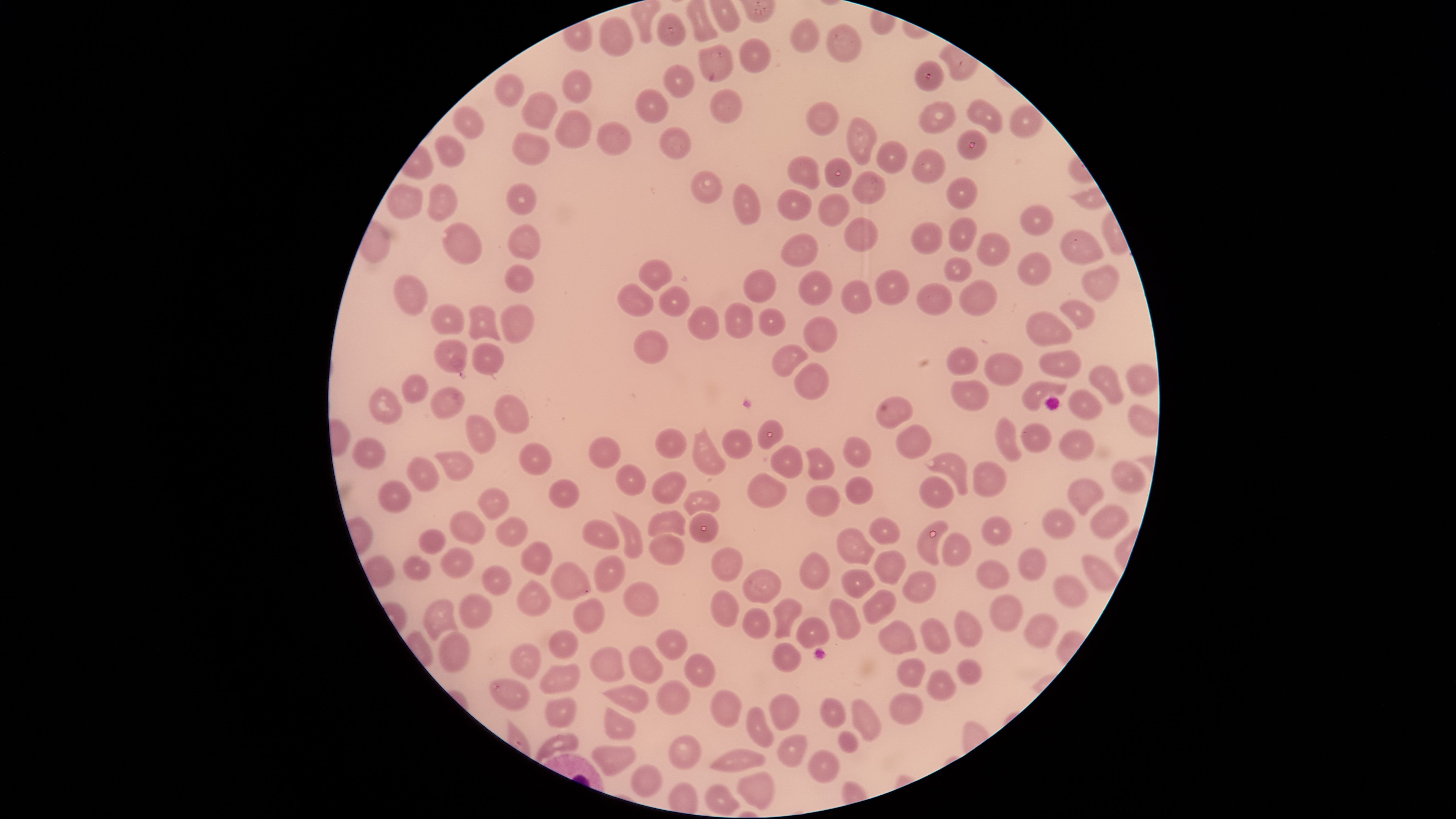 Approximate bounding boxes as [left, top, right, bottom] in pixels. Uninfected red blood cells: [655, 11, 687, 48], [599, 15, 634, 57], [788, 16, 820, 53], [825, 23, 863, 64], [739, 37, 771, 74], [696, 43, 734, 84], [914, 59, 945, 93], [662, 64, 695, 98], [561, 69, 593, 104], [493, 72, 525, 108], [635, 87, 669, 124], [710, 88, 742, 124], [520, 90, 559, 130], [967, 98, 1003, 134], [806, 101, 841, 136], [917, 101, 958, 134], [451, 104, 486, 141], [1007, 104, 1045, 140], [553, 109, 592, 149], [845, 117, 878, 166], [596, 121, 633, 157], [659, 125, 692, 160], [957, 129, 988, 161], [511, 131, 551, 166], [433, 134, 466, 168], [875, 139, 909, 174], [911, 146, 946, 183], [786, 155, 820, 191], [824, 156, 853, 187], [851, 170, 886, 205], [690, 171, 724, 205], [946, 177, 979, 210], [384, 182, 424, 220], [504, 182, 538, 217], [731, 182, 762, 225], [426, 183, 459, 222], [776, 188, 814, 221], [817, 193, 851, 228], [1019, 204, 1054, 236], [844, 216, 879, 253], [947, 217, 978, 252], [441, 220, 483, 265], [911, 221, 943, 254], [506, 223, 541, 261], [1059, 229, 1105, 264], [976, 231, 1011, 267], [779, 233, 818, 267], [1016, 251, 1053, 286], [944, 256, 973, 284], [638, 259, 673, 292], [504, 262, 536, 294], [1081, 264, 1120, 304], [742, 269, 777, 304], [875, 269, 910, 306], [798, 270, 834, 306], [393, 273, 429, 316], [840, 278, 873, 315], [958, 278, 999, 317], [616, 282, 655, 317], [915, 282, 953, 316], [658, 285, 691, 317], [1058, 299, 1096, 329], [723, 301, 755, 338], [429, 302, 464, 335], [499, 303, 536, 343], [468, 304, 502, 341], [687, 305, 720, 341], [758, 307, 786, 336], [1025, 310, 1074, 347], [802, 315, 840, 353], [632, 328, 669, 364], [432, 339, 467, 373], [471, 343, 505, 376], [771, 344, 809, 377], [946, 346, 980, 376], [1039, 348, 1082, 379], [983, 351, 1024, 387], [793, 361, 830, 399], [1124, 362, 1158, 396], [1087, 364, 1125, 406], [401, 373, 429, 404], [950, 379, 990, 412], [1021, 381, 1068, 412], [367, 386, 404, 425], [430, 386, 466, 419], [1067, 388, 1103, 421], [493, 394, 530, 434], [875, 395, 914, 429], [464, 413, 497, 453], [994, 416, 1022, 463], [757, 418, 784, 450], [1019, 422, 1053, 454], [691, 423, 727, 477], [896, 423, 932, 459], [654, 427, 688, 459], [721, 428, 753, 461], [1058, 429, 1096, 462], [842, 435, 873, 468], [351, 436, 386, 470], [588, 436, 622, 470], [518, 442, 553, 476], [770, 444, 804, 479], [805, 446, 836, 481], [433, 449, 475, 482], [923, 451, 968, 496], [405, 456, 441, 493], [1109, 459, 1148, 493], [972, 460, 1008, 497], [615, 463, 647, 496], [651, 470, 687, 504], [746, 472, 787, 509], [844, 475, 874, 506], [918, 476, 957, 509], [1065, 477, 1105, 516], [548, 478, 580, 509], [378, 480, 412, 513], [804, 485, 842, 517], [475, 487, 510, 521], [683, 491, 720, 516], [1089, 503, 1129, 540], [1041, 508, 1078, 541], [647, 509, 687, 538], [448, 510, 486, 545], [610, 510, 644, 559], [688, 512, 720, 543], [981, 514, 1014, 548], [494, 515, 529, 547], [868, 516, 902, 545], [582, 519, 621, 550], [916, 519, 950, 567], [836, 525, 876, 565], [417, 528, 446, 555], [941, 530, 972, 568], [647, 533, 686, 565], [520, 540, 552, 576], [439, 546, 475, 579], [710, 546, 744, 583], [1017, 546, 1048, 581], [872, 550, 906, 585], [800, 552, 831, 592], [1080, 552, 1120, 592], [592, 554, 626, 594], [402, 555, 432, 581], [976, 558, 1011, 590], [550, 560, 591, 601], [480, 564, 513, 596], [742, 568, 782, 605], [841, 568, 876, 600], [902, 570, 937, 604], [1051, 574, 1090, 609], [516, 579, 552, 617], [623, 580, 660, 619], [709, 589, 740, 628], [861, 589, 898, 625], [457, 592, 493, 629], [988, 594, 1023, 633], [828, 597, 862, 641], [421, 598, 460, 641], [571, 598, 605, 635], [771, 598, 804, 639], [741, 607, 772, 640], [953, 610, 983, 648], [1022, 613, 1060, 648], [795, 616, 830, 649], [920, 617, 952, 655], [877, 620, 918, 655], [654, 627, 689, 661], [547, 629, 579, 661], [439, 631, 471, 674], [509, 642, 542, 681], [771, 642, 803, 673], [627, 644, 664, 685], [589, 645, 626, 683], [682, 652, 717, 688], [895, 657, 927, 689], [955, 658, 983, 685], [539, 663, 582, 694], [926, 668, 958, 703], [488, 678, 532, 711], [656, 679, 692, 716], [600, 683, 649, 714], [709, 688, 743, 728], [769, 692, 801, 732], [888, 692, 924, 726], [543, 696, 577, 729], [819, 697, 846, 729], [850, 698, 882, 742], [603, 705, 637, 741], [746, 705, 775, 749], [837, 729, 859, 754], [534, 732, 579, 763], [776, 733, 807, 768], [667, 735, 702, 770], [590, 744, 637, 776], [708, 747, 766, 773], [807, 749, 841, 784], [629, 763, 664, 798], [736, 770, 774, 811], [704, 783, 742, 816]. Single field of view. Giemsa-stained preparation. Presence: no malaria parasites detected. Image is 1456×819 pixels. The visible region is circular. Photographed with a smartphone camera through the microscope eyepiece. Thin blood smear.